Classify this cell by malaria status.
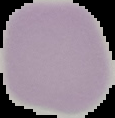

It is uninfected.

image type = segmented cell region on a black background
preparation = thin blood smear
image size = 115×118 pixels